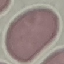

Summary:
  - Malaria status: uninfected
  - Capture: smartphone camera at the microscope eyepiece
  - Preparation: thin blood smear
  - Image type: automatically extracted cell patch, resized to 64 × 64 pixels
  - Stain: Giemsa